Identify the parasite.
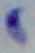

This is Toxoplasma gondii.

Summary:
  - Magnification: 1000x
  - Modality: micrograph